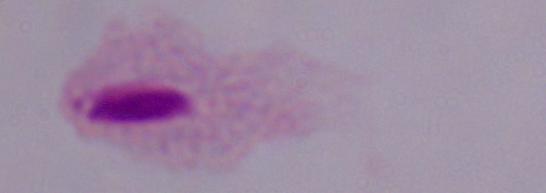
Summary:
  - Modality: micrograph
  - Identification: trichomonad
  - Magnification: 1000x